Locate and identify every blood parasite.
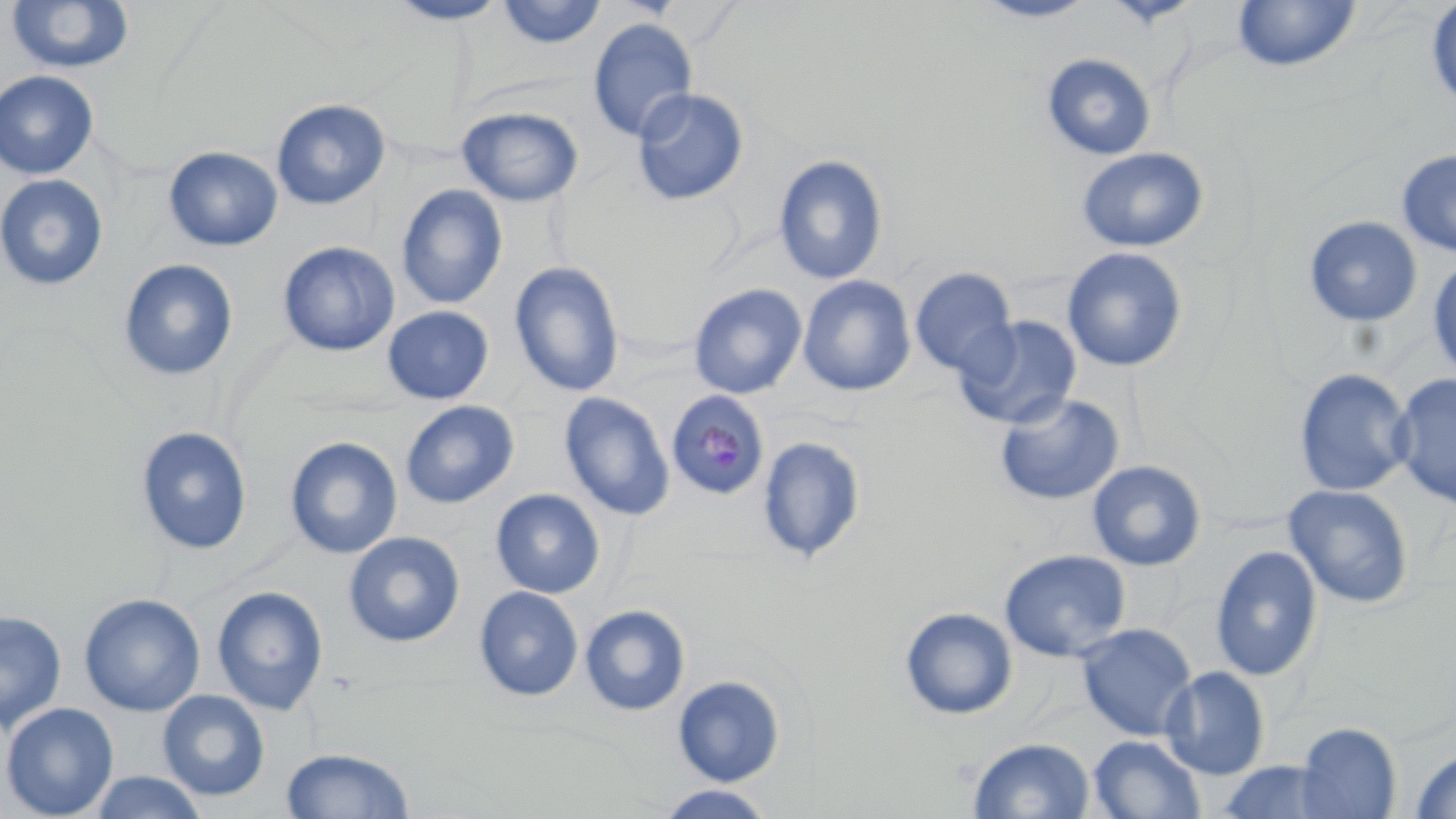
Approximate bounding boxes as named x1/y1/x2/y2 corners in pixels.
Plasmodium malariae-infected red blood cells: (x1=666, y1=389, x2=770, y2=501).
No Plasmodium falciparum, Plasmodium ovale, Plasmodium vivax, Babesia divergens, or Trypanosoma brucei observed.

Uninfected red blood cell locations: (x1=384, y1=0, x2=511, y2=25), (x1=974, y1=0, x2=1099, y2=23), (x1=5, y1=1, x2=135, y2=76), (x1=496, y1=1, x2=608, y2=49), (x1=1232, y1=1, x2=1361, y2=73), (x1=1426, y1=1, x2=1456, y2=113), (x1=587, y1=18, x2=698, y2=142), (x1=1041, y1=53, x2=1157, y2=161), (x1=0, y1=70, x2=100, y2=180), (x1=631, y1=88, x2=750, y2=207), (x1=271, y1=98, x2=391, y2=210), (x1=456, y1=106, x2=584, y2=207), (x1=163, y1=146, x2=283, y2=252), (x1=1076, y1=147, x2=1210, y2=253), (x1=1396, y1=149, x2=1456, y2=258), (x1=773, y1=155, x2=888, y2=285), (x1=0, y1=174, x2=109, y2=291), (x1=396, y1=185, x2=508, y2=309), (x1=1303, y1=215, x2=1423, y2=327), (x1=278, y1=241, x2=400, y2=357), (x1=1061, y1=246, x2=1188, y2=373), (x1=118, y1=258, x2=239, y2=381), (x1=1428, y1=259, x2=1456, y2=383), (x1=510, y1=261, x2=625, y2=398), (x1=909, y1=268, x2=1017, y2=378), (x1=797, y1=275, x2=915, y2=396), (x1=688, y1=283, x2=807, y2=399), (x1=382, y1=305, x2=494, y2=405), (x1=954, y1=316, x2=1082, y2=429), (x1=1294, y1=368, x2=1414, y2=497), (x1=1390, y1=372, x2=1456, y2=509), (x1=558, y1=392, x2=676, y2=521), (x1=995, y1=393, x2=1124, y2=506), (x1=400, y1=400, x2=520, y2=509), (x1=135, y1=426, x2=253, y2=556), (x1=284, y1=436, x2=403, y2=560), (x1=757, y1=436, x2=866, y2=563), (x1=1086, y1=460, x2=1206, y2=572), (x1=1283, y1=484, x2=1414, y2=608), (x1=491, y1=489, x2=605, y2=598), (x1=343, y1=531, x2=465, y2=648), (x1=1210, y1=545, x2=1323, y2=681), (x1=999, y1=549, x2=1131, y2=662), (x1=211, y1=585, x2=329, y2=716), (x1=474, y1=586, x2=583, y2=701), (x1=79, y1=593, x2=205, y2=717), (x1=579, y1=604, x2=690, y2=716), (x1=900, y1=607, x2=1018, y2=720), (x1=0, y1=610, x2=67, y2=735), (x1=1075, y1=623, x2=1197, y2=741), (x1=1160, y1=666, x2=1270, y2=779), (x1=672, y1=675, x2=785, y2=786), (x1=157, y1=690, x2=270, y2=801), (x1=0, y1=702, x2=120, y2=819), (x1=1295, y1=723, x2=1401, y2=819), (x1=1088, y1=735, x2=1206, y2=819), (x1=968, y1=737, x2=1095, y2=819), (x1=280, y1=747, x2=416, y2=818), (x1=1408, y1=747, x2=1456, y2=819), (x1=1213, y1=761, x2=1349, y2=819), (x1=87, y1=770, x2=210, y2=819), (x1=654, y1=784, x2=779, y2=819). Slide-level diagnosis: Plasmodium malariae. Single field of view. Image is 1456×819 pixels. Thin blood smear. Captured at 1000x magnification. May-Grünwald-Giemsa stain. Optical microscopy.